Name the parasite shown.
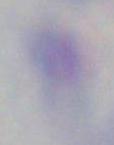

This is Toxoplasma gondii.

Summary:
  - Modality: micrograph
  - Magnification: 1000x